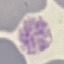
result: malaria parasites detected
image_type: cell patch, automatically extracted from a larger field of view and resized to 64 × 64 pixels
capture: smartphone camera at the microscope eyepiece
preparation: thin blood film
stain: Giemsa